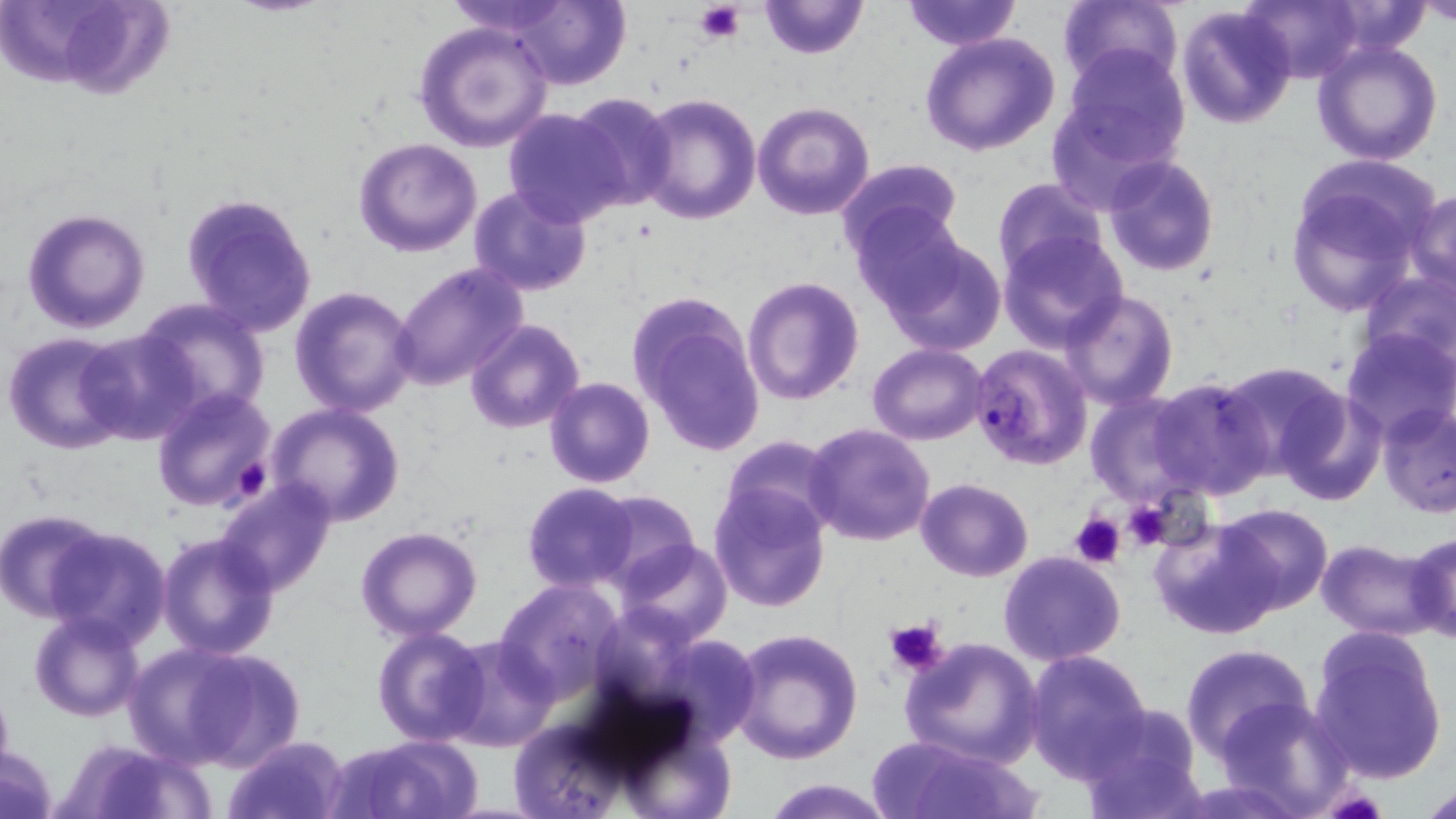

slide-level diagnosis = Plasmodium falciparum
platelet locations = approximate bounding boxes as (x1, y1, x2, y2) in pixels: (694, 1, 746, 44), (223, 452, 273, 503), (1121, 501, 1173, 553), (1070, 512, 1125, 568), (882, 618, 948, 677)
field of view = one of a larger specimen
stain = May-Grünwald-Giemsa
image size = 1456×819 pixels
uninfected red blood cell locations = approximate bounding boxes as (x1, y1, x2, y2) in pixels: (37, 0, 176, 104), (758, 0, 868, 59), (901, 0, 1022, 49), (1057, 0, 1184, 91), (1242, 0, 1363, 84), (1419, 0, 1455, 27), (502, 1, 630, 89), (1324, 3, 1431, 52), (1176, 5, 1298, 130), (413, 20, 555, 152), (920, 31, 1061, 156), (1311, 39, 1444, 167), (1061, 45, 1190, 166), (566, 91, 678, 212), (637, 92, 762, 226), (752, 101, 874, 219), (502, 109, 627, 227), (354, 137, 483, 257), (1102, 154, 1219, 277), (834, 157, 965, 259), (1285, 167, 1430, 312), (991, 178, 1107, 279), (468, 184, 593, 297), (1408, 191, 1456, 295), (180, 192, 318, 337), (852, 204, 970, 315), (22, 207, 150, 333), (870, 229, 1008, 356), (998, 230, 1125, 349), (390, 262, 531, 389), (1358, 266, 1456, 372), (742, 276, 865, 406), (288, 285, 421, 416), (1061, 290, 1179, 409), (627, 294, 765, 458), (134, 298, 267, 421), (463, 318, 585, 435), (73, 328, 197, 445), (1338, 330, 1456, 444), (3, 332, 133, 455), (867, 344, 990, 445), (1216, 359, 1352, 478), (1148, 375, 1276, 499), (543, 376, 656, 488), (151, 386, 277, 513), (1274, 387, 1386, 505), (1086, 392, 1202, 503), (1378, 401, 1456, 518), (267, 404, 406, 527), (803, 423, 936, 548), (721, 434, 840, 536), (915, 477, 1034, 581), (215, 481, 336, 596), (523, 482, 639, 593), (709, 484, 830, 612), (588, 490, 699, 589), (1213, 504, 1333, 616), (2, 508, 108, 621), (1151, 518, 1283, 639), (45, 525, 171, 647), (356, 527, 483, 642), (1405, 531, 1456, 645), (156, 533, 281, 660), (616, 538, 732, 644), (1317, 539, 1444, 639), (998, 551, 1127, 665), (494, 579, 623, 702), (27, 610, 147, 722), (726, 626, 863, 765), (373, 627, 489, 746), (1308, 628, 1448, 784), (649, 632, 761, 747), (440, 637, 557, 752), (900, 637, 1043, 768), (131, 644, 297, 771), (1179, 644, 1315, 762), (1024, 648, 1153, 780), (0, 677, 14, 785), (1223, 696, 1356, 815), (1078, 704, 1207, 819), (508, 719, 626, 814), (221, 735, 348, 819), (340, 735, 482, 819), (877, 735, 1041, 819), (66, 740, 213, 818), (1, 744, 58, 819), (763, 778, 893, 818), (1419, 784, 1456, 818)
magnification = 1000x
Plasmodium falciparum-infected red blood cell locations = approximate bounding boxes as (x1, y1, x2, y2) in pixels: (969, 341, 1093, 470)
modality = light microscopy
preparation = thin blood smear